Point out each Plasmodium parasite.
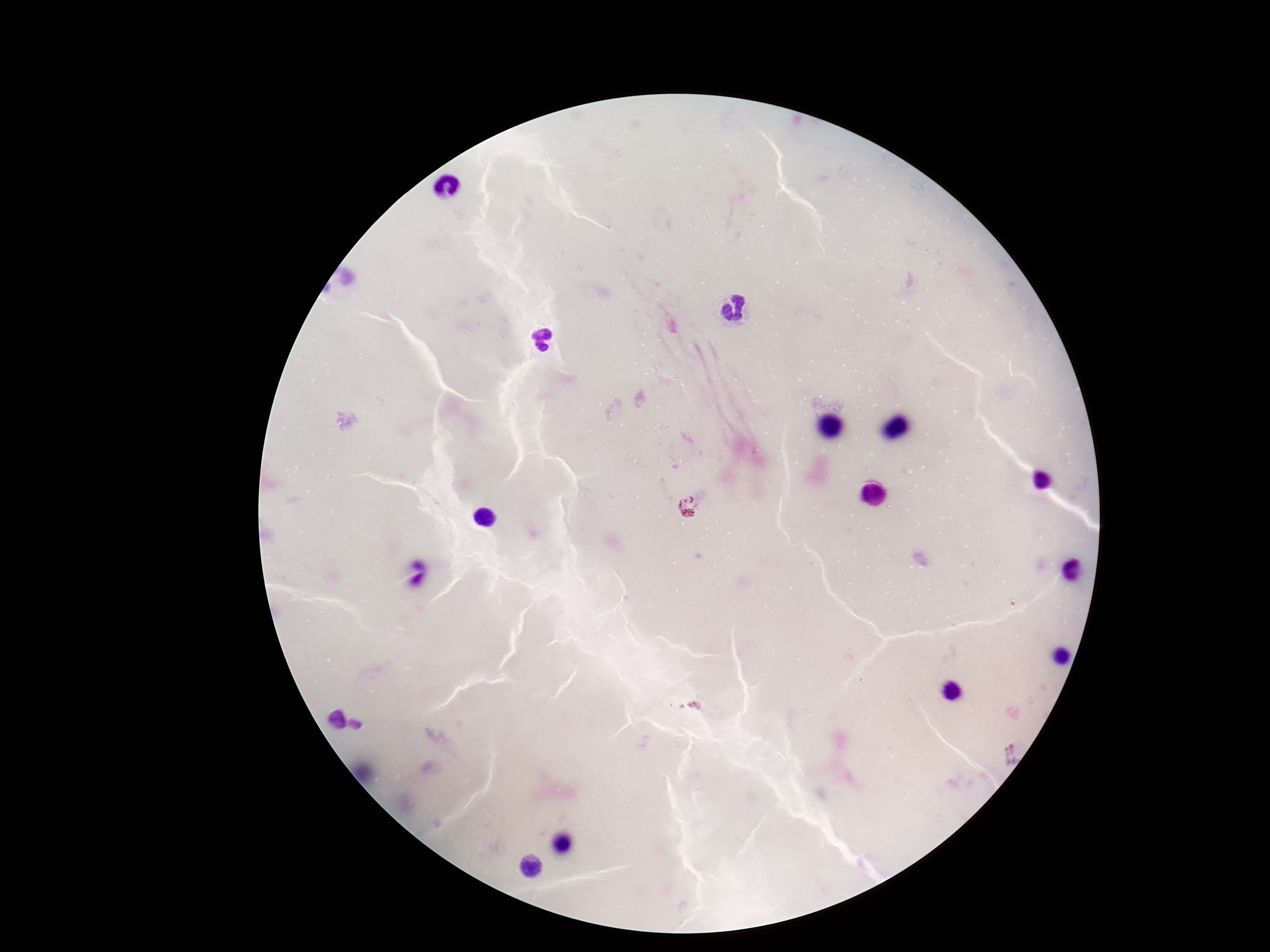

Approximate centers as [x, y] in pixels.
Plasmodium parasites: [689, 506], [333, 718], [359, 724].

Summary:
  - Stain: Giemsa
  - Preparation: thick blood smear
  - Magnification: 100x
  - Field of view: one from this slide
  - Patient malaria status: infected
  - Image size: 1270×952 pixels
  - Capture: smartphone camera through the microscope eyepiece